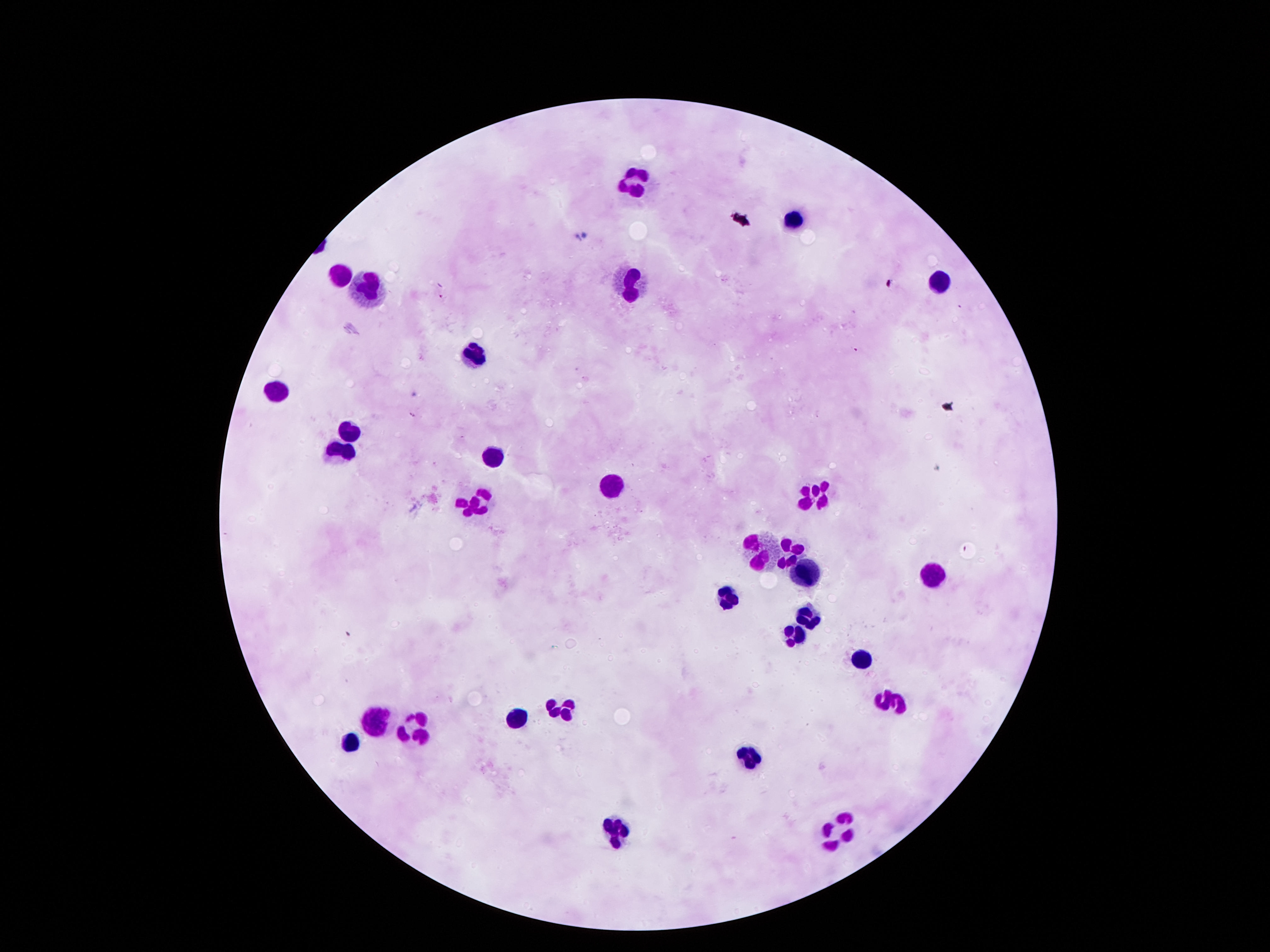

Approximate centers as (x, y) in pixels.
Summary:
  - Leukocyte locations: (635, 182), (339, 276), (937, 279), (372, 280), (632, 287), (479, 359), (281, 390), (350, 429), (496, 456), (332, 461), (613, 483), (821, 490), (474, 505), (791, 548), (764, 555), (805, 575), (932, 575), (728, 599), (803, 618), (789, 640), (860, 659), (895, 704), (554, 707), (372, 718), (510, 722), (413, 724), (348, 740), (755, 758), (834, 828), (618, 832)
  - Stain: Giemsa
  - Image size: 1270×952 pixels
  - Preparation: thick peripheral-blood smear
  - Capture: smartphone camera through the microscope eyepiece
  - Field of view: one from this slide
  - Magnification: 100x
  - Patient malaria status: uninfected